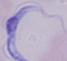

modality: photomicrograph
identification: trypanosome
magnification: 1000x